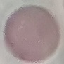

Result: negative for malaria parasites. Thin blood smear. Automatically extracted cell patch, resized to 64 × 64 pixels. Acquired by smartphone through the microscope eyepiece. Giemsa stain.